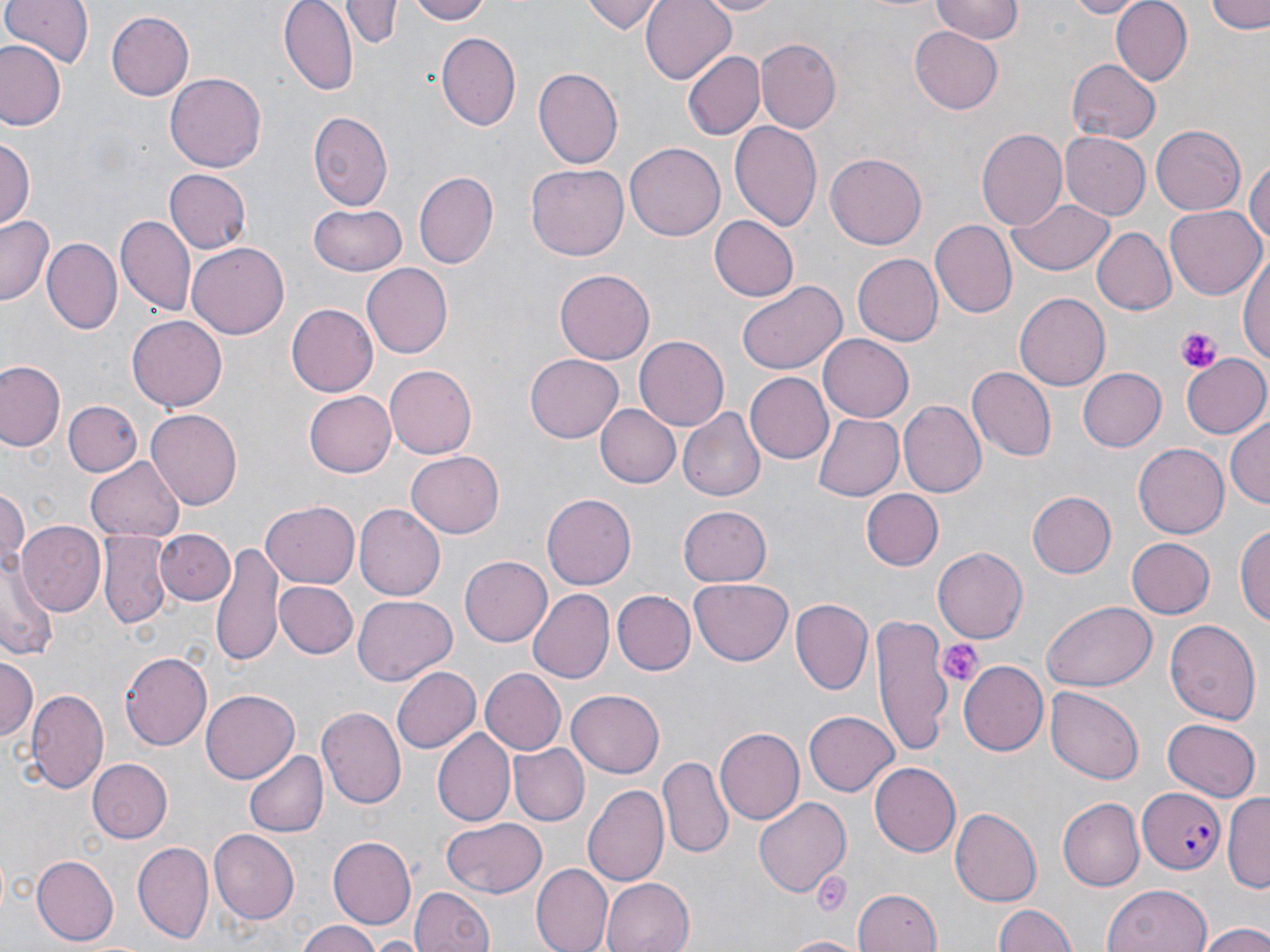
Approximate bounding boxes as (x1,y1)-(x2,y2) corner pairs in pixels. Plasmodium falciparum-infected red blood cell locations: (1135,786)-(1228,873). Platelet locations: (1177,328)-(1218,371), (938,639)-(982,686), (812,871)-(851,918). Uninfected red blood cell locations: (1,0)-(94,70), (344,0)-(397,50), (409,0)-(493,25), (584,0)-(665,34), (641,0)-(738,83), (696,0)-(786,16), (931,0)-(1022,42), (1065,0)-(1143,18), (1109,0)-(1193,86), (1208,0)-(1270,35), (281,1)-(355,92), (106,9)-(194,101), (909,28)-(1004,113), (438,33)-(521,129), (756,39)-(841,133), (0,41)-(66,131), (681,49)-(764,140), (1065,58)-(1159,145), (533,68)-(622,170), (166,73)-(265,174), (308,113)-(393,210), (729,121)-(822,231), (1150,124)-(1245,216), (976,129)-(1068,233), (1059,130)-(1150,218), (1,135)-(35,235), (625,142)-(725,240), (825,153)-(926,248), (1247,154)-(1269,256), (527,164)-(629,260), (163,169)-(249,255), (413,172)-(496,269), (1008,199)-(1116,276), (307,203)-(408,279), (1166,203)-(1265,296), (1,214)-(56,307), (116,215)-(195,316), (708,216)-(799,302), (931,219)-(1018,319), (1091,228)-(1176,315), (44,237)-(121,334), (188,241)-(290,338), (1238,253)-(1270,366), (850,254)-(942,346), (360,263)-(452,358), (552,267)-(656,366), (738,280)-(846,374), (1015,292)-(1111,390), (286,304)-(379,397), (127,316)-(226,410), (818,334)-(913,422), (634,337)-(727,428), (1182,353)-(1270,440), (524,354)-(624,443), (0,361)-(64,452), (384,365)-(477,458), (965,367)-(1053,459), (1075,367)-(1164,452), (743,371)-(834,463), (305,388)-(400,477), (63,400)-(143,477), (899,402)-(986,498), (596,404)-(680,488), (677,408)-(765,502), (147,409)-(243,510), (813,413)-(906,501), (1227,414)-(1270,507), (1133,440)-(1228,535), (406,449)-(503,537), (85,455)-(183,540), (1,486)-(28,577), (859,489)-(942,571), (1026,491)-(1114,578), (542,494)-(636,589), (261,501)-(358,589), (356,504)-(445,601), (678,506)-(771,587), (1235,520)-(1269,630), (16,522)-(105,617), (158,528)-(233,605), (100,534)-(169,630), (1126,537)-(1215,618), (211,542)-(285,667), (933,547)-(1027,643), (459,555)-(553,647), (2,558)-(57,662), (690,578)-(793,666), (276,580)-(358,660), (526,588)-(615,682), (613,590)-(695,675), (353,596)-(455,684), (790,597)-(874,697), (1044,602)-(1156,690), (870,615)-(953,756), (1164,617)-(1262,722), (120,651)-(213,750), (0,655)-(37,745), (961,660)-(1049,754), (390,666)-(481,754), (479,669)-(565,754), (1047,686)-(1144,783), (27,687)-(108,792), (201,690)-(298,781), (568,691)-(663,777), (316,707)-(406,810), (804,709)-(899,796), (1161,718)-(1261,800), (714,729)-(803,825), (433,730)-(513,824), (508,742)-(587,825), (244,749)-(328,839), (658,755)-(733,859), (87,758)-(173,843), (868,762)-(959,856), (583,784)-(669,888), (1225,790)-(1270,892), (755,796)-(850,897), (1058,797)-(1145,891), (950,808)-(1041,905), (441,816)-(549,897), (210,828)-(302,924), (327,835)-(416,926), (133,843)-(213,943), (30,855)-(118,944), (532,865)-(612,951), (600,878)-(691,952), (1103,883)-(1213,952), (411,886)-(493,952), (852,889)-(941,952), (993,904)-(1078,952), (297,923)-(385,952), (1198,923)-(1270,952), (782,935)-(862,952), (370,939)-(422,950). Slide-level diagnosis: Plasmodium falciparum. Optical microscopy. Image is 1270×952 pixels. May-Grünwald-Giemsa stain. 1000x magnification. Thin blood smear. One field of a larger specimen.